Name the blood parasite species.
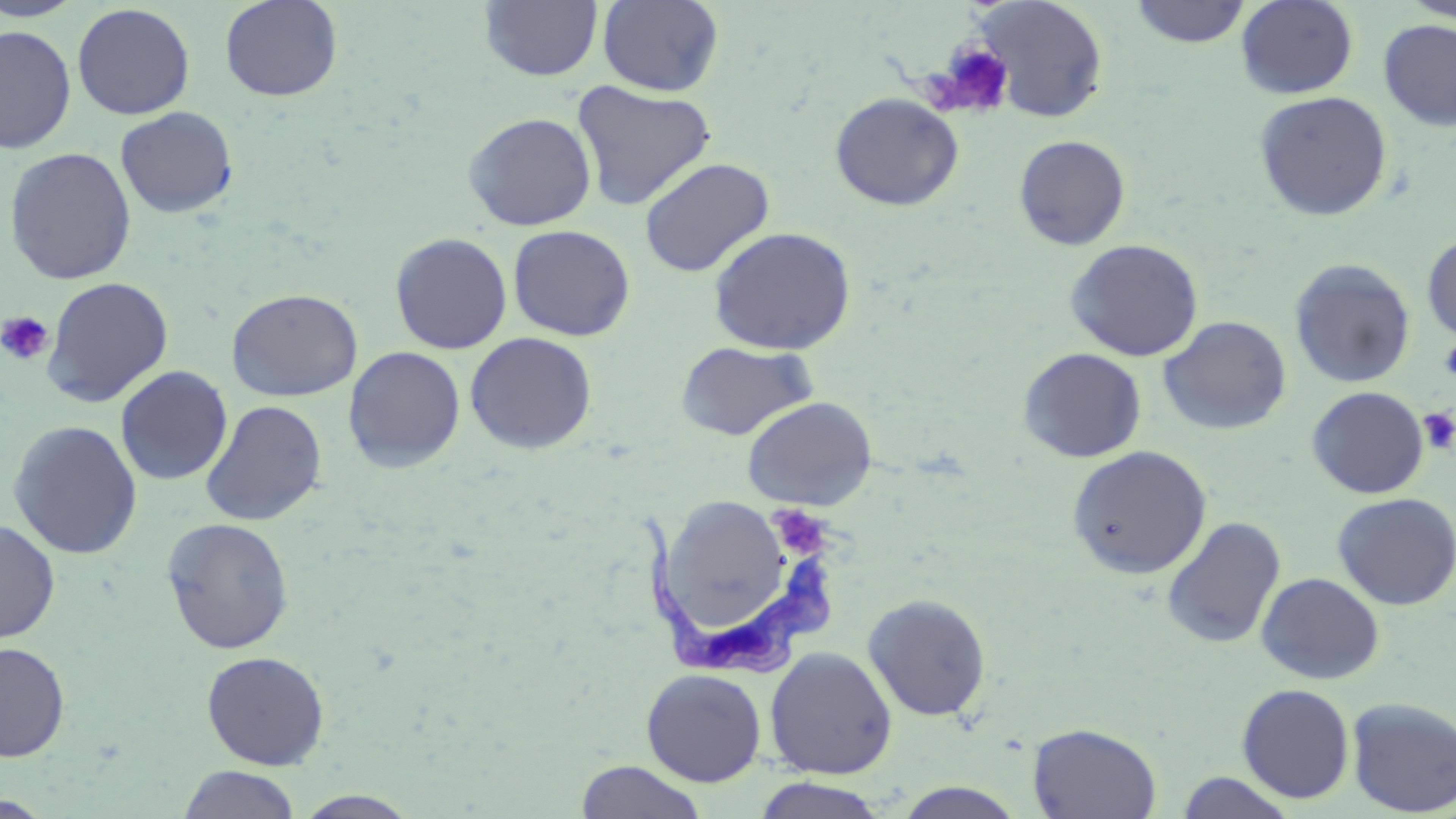

Trypanosoma brucei.

field of view = one of a larger specimen
Trypanosoma brucei locations = approximate bounding boxes as (x1, y1, x2, y2) in pixels: (634, 511, 833, 679)
stain = May-Grünwald-Giemsa
magnification = 1000x
image size = 1456×819 pixels
platelet locations = approximate bounding boxes as (x1, y1, x2, y2) in pixels: (933, 42, 1015, 118), (0, 311, 54, 366), (1439, 337, 1456, 383), (1418, 408, 1456, 455), (770, 505, 833, 559)
uninfected red blood cell locations = approximate bounding boxes as (x1, y1, x2, y2) in pixels: (219, 0, 343, 102), (597, 0, 724, 96), (973, 0, 1109, 123), (1236, 0, 1358, 99), (1400, 0, 1456, 23), (0, 1, 88, 22), (480, 1, 603, 81), (1129, 1, 1251, 48), (71, 3, 195, 120), (1378, 19, 1456, 131), (0, 24, 77, 153), (572, 81, 716, 210), (1254, 91, 1392, 221), (830, 92, 963, 210), (115, 106, 238, 218), (463, 112, 597, 231), (1014, 135, 1130, 250), (3, 147, 137, 284), (639, 157, 774, 277), (508, 224, 635, 341), (708, 226, 857, 356), (1422, 231, 1456, 344), (390, 232, 512, 354), (1065, 238, 1203, 361), (1289, 259, 1416, 388), (42, 276, 173, 407), (226, 288, 362, 401), (1158, 316, 1291, 435), (464, 332, 597, 454), (674, 340, 819, 441), (343, 346, 466, 472), (1018, 347, 1146, 463), (115, 366, 233, 486), (1307, 386, 1429, 499), (742, 396, 877, 511), (201, 400, 327, 526), (7, 420, 143, 559), (1067, 445, 1211, 579), (649, 491, 787, 630), (1331, 492, 1456, 610), (1161, 516, 1286, 650), (162, 517, 294, 654), (0, 518, 60, 643), (1256, 572, 1384, 684), (862, 593, 992, 721), (0, 641, 70, 762), (764, 647, 897, 779), (201, 651, 330, 769), (641, 668, 767, 786), (1237, 683, 1355, 804), (1346, 697, 1456, 816), (1027, 723, 1162, 819), (575, 760, 709, 819), (178, 765, 302, 819), (1175, 772, 1297, 818), (751, 777, 891, 818), (892, 782, 1028, 818), (293, 790, 422, 818), (0, 795, 53, 818)
modality = optical microscopy
preparation = thin blood film